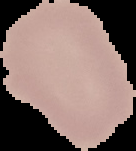
image size = 136×151 pixels
preparation = thin blood smear
result = negative for Plasmodium parasites
image type = segmented cell region with the area outside set to black